Comment on the morphology of the erythrocytes.
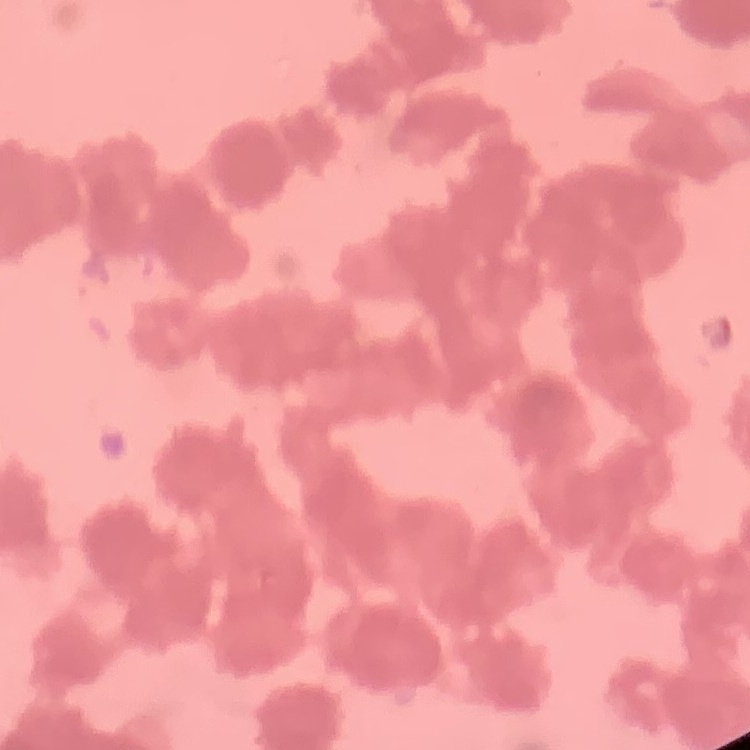
Rouleaux formation.

Summary:
  - Image type: square crop of a larger photomicrograph
  - Stain: Field's or Giemsa
  - Preparation: thin blood smear